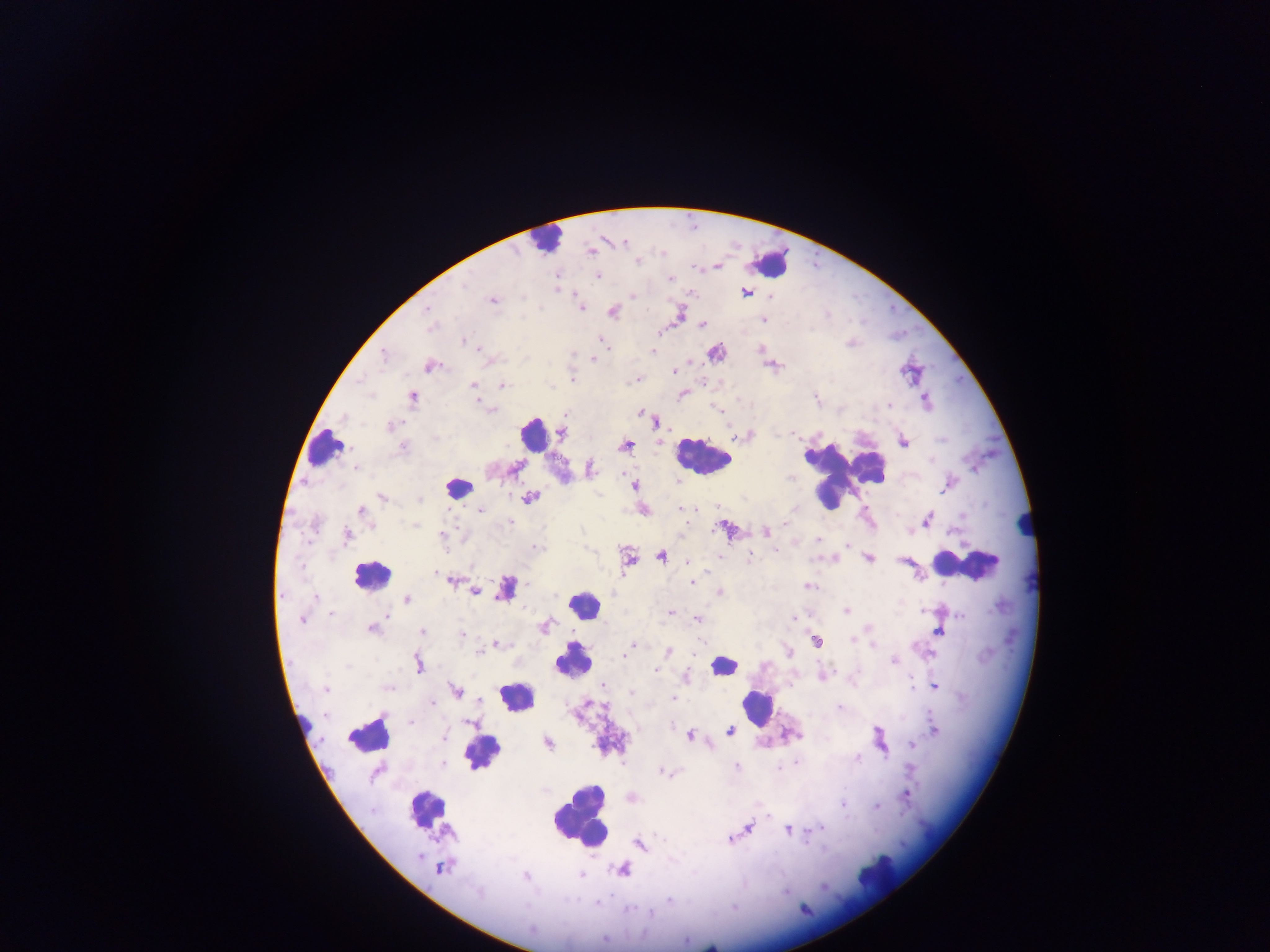

{
  "country": "Ghana",
  "plasmodium_parasite_locations": "approximate centers as x y in pixels: 624 243; 663 252; 639 263; 597 276; 670 279; 465 285; 557 290; 631 297; 771 297; 492 301; 427 308; 582 308; 764 320; 702 324; 663 333; 600 338; 464 340; 482 351; 654 352; 383 356; 593 360; 702 364; 427 366; 674 370; 573 376; 637 377; 501 384; 471 386; 413 396; 478 402; 888 406; 390 425; 402 448; 622 473; 680 508; 480 511; 360 512; 510 520; 793 525; 716 529; 442 535; 310 539; 819 540; 846 543; 777 551; 749 557; 716 558; 687 560; 300 567; 435 573; 691 583; 807 584; 313 597; 500 598; 329 614; 670 614; 960 616; 794 617; 385 618; 696 618; 301 620; 370 630; 422 630; 464 636; 701 640; 496 646; 671 652; 478 653; 624 656; 893 660; 654 670; 911 683; 390 687; 325 690; 632 694; 673 698; 434 703; 838 707; 412 721; 443 735; 796 762; 442 765; 737 766; 780 769; 664 773; 907 797; 844 806; 877 807; 766 813; 818 829; 787 830; 730 838; 806 844; 439 867; 582 876; 526 879; 477 894; 611 894; 669 899; 596 902; 626 909; 651 914; 605 939",
  "preparation": "thick blood smear",
  "leukocyte_locations": "approximate centers as x y in pixels: 543 239; 774 263; 529 433; 325 449; 700 457; 845 473; 452 485; 968 560; 370 573; 585 602; 570 665; 515 700; 756 707; 367 735; 425 806; 577 822",
  "field_of_view": "single",
  "image_size": "1270×952 pixels",
  "capture": "mobile-phone photograph through a microscope"
}